Report the malaria status of this cell.
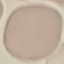
Uninfected.

{
  "image_type": "cell patch, automatically extracted from a larger field of view and resized to 64 × 64 pixels",
  "capture": "smartphone through the microscope eyepiece",
  "preparation": "thin smear",
  "stain": "Giemsa"
}